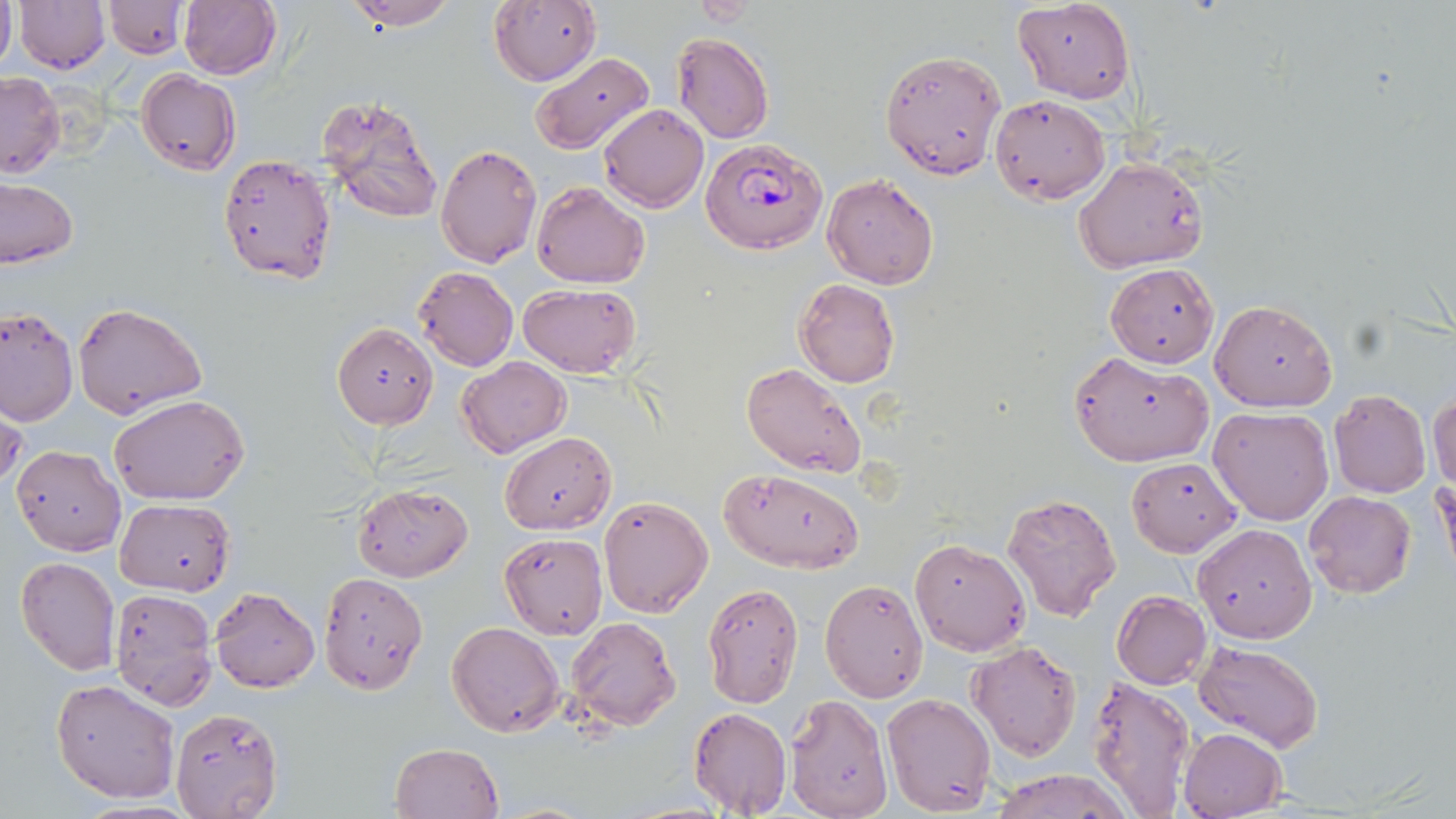
Summary:
  - Coordinate format: approximate bounding boxes as (x1, y1, x2, y2) in pixels
  - Uninfected red blood cell locations: (0, 0, 15, 76), (13, 0, 110, 73), (177, 0, 281, 81), (343, 0, 460, 29), (488, 0, 600, 86), (686, 0, 762, 23), (104, 1, 187, 59), (1014, 1, 1134, 103), (671, 32, 774, 144), (879, 47, 1006, 179), (530, 52, 656, 156), (136, 70, 240, 176), (1, 71, 64, 178), (316, 93, 443, 225), (990, 95, 1109, 204), (596, 103, 709, 213), (435, 144, 542, 268), (218, 153, 337, 285), (1074, 158, 1205, 274), (822, 174, 941, 291), (0, 178, 77, 267), (531, 180, 650, 288), (1105, 262, 1219, 367), (412, 265, 519, 372), (793, 278, 900, 388), (517, 283, 641, 378), (1210, 300, 1337, 412), (73, 302, 206, 420), (0, 306, 76, 426), (333, 323, 438, 428), (1068, 352, 1212, 467), (457, 357, 571, 457), (741, 362, 870, 478), (1329, 390, 1430, 497), (1429, 391, 1456, 492), (110, 392, 251, 505), (0, 395, 26, 499), (1208, 407, 1333, 524), (500, 432, 616, 533), (12, 445, 126, 556), (1128, 456, 1241, 556), (718, 469, 864, 573), (1435, 472, 1455, 577), (352, 483, 472, 581), (1304, 491, 1415, 599), (1002, 492, 1123, 620), (598, 494, 713, 618), (115, 499, 235, 597), (1193, 522, 1316, 643), (499, 532, 608, 640), (911, 538, 1030, 655), (15, 556, 120, 675), (318, 572, 428, 693), (818, 578, 929, 702), (700, 582, 804, 708), (210, 586, 319, 693), (108, 587, 217, 708), (1111, 592, 1211, 690), (565, 616, 681, 731), (445, 621, 564, 738), (968, 640, 1084, 760), (1195, 641, 1323, 751), (1088, 674, 1197, 816), (51, 678, 181, 804), (882, 691, 996, 813), (783, 694, 893, 819), (168, 707, 283, 819), (688, 707, 793, 814), (1180, 728, 1286, 819), (389, 742, 503, 819), (990, 768, 1132, 819)
  - Plasmodium falciparum-infected red blood cell locations: (701, 135, 828, 256)
  - Slide-level diagnosis: Plasmodium falciparum
  - Image size: 1456×819 pixels
  - Field of view: one of a larger specimen
  - Stain: May-Grünwald-Giemsa
  - Magnification: 1000x
  - Modality: light microscopy
  - Preparation: thin blood film